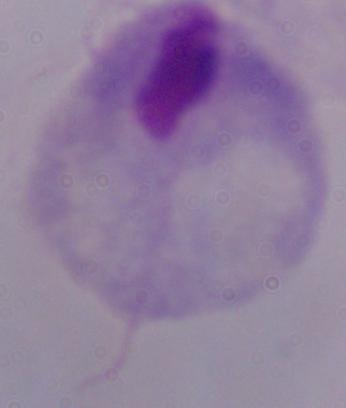

Summary:
  - Modality: photomicrograph
  - Identification: trichomonad
  - Magnification: 1000x